State the blood parasite species.
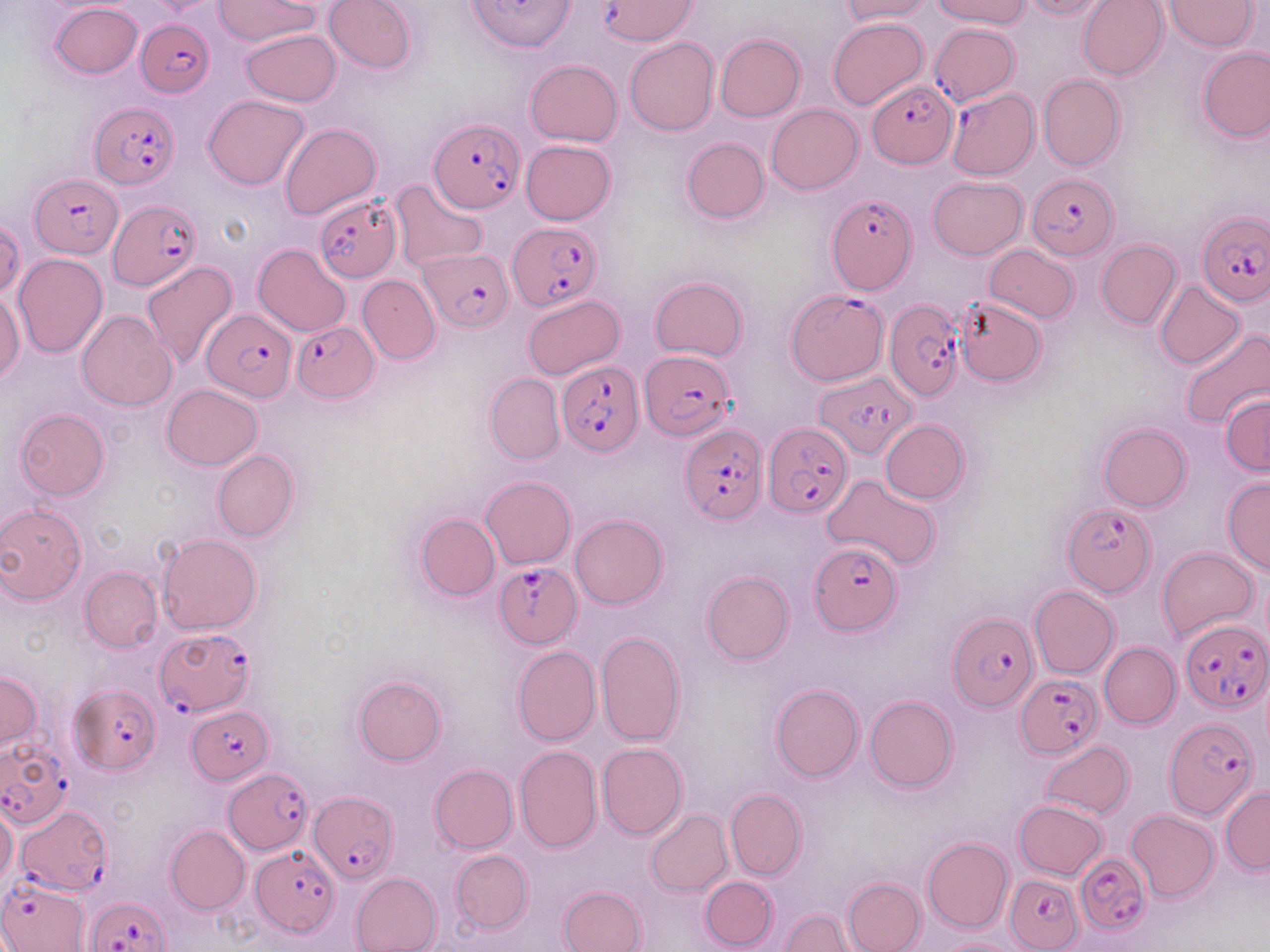

Plasmodium falciparum.

stain = May-Grünwald-Giemsa
image size = 1270×952 pixels
field of view = single
modality = light microscopy
Plasmodium falciparum-infected red blood cell locations = approximate bounding boxes as (x1,y1)-(x2,y2) corner pairs in pixels: (597,2)-(698,50), (136,18)-(213,98), (929,23)-(1019,105), (867,79)-(956,166), (946,88)-(1038,180), (88,101)-(180,188), (429,118)-(525,214), (1027,173)-(1119,260), (32,174)-(123,257), (313,194)-(402,281), (828,194)-(917,295), (109,199)-(200,290), (1198,214)-(1269,306), (507,223)-(600,311), (421,247)-(511,331), (785,290)-(889,385), (884,298)-(967,401), (201,308)-(298,401), (294,322)-(376,402), (643,351)-(735,441), (555,359)-(644,456), (815,375)-(915,459), (763,421)-(852,519), (680,424)-(767,523), (1062,502)-(1156,596), (809,544)-(902,634), (494,563)-(582,648), (950,612)-(1037,711), (1179,616)-(1269,715), (156,628)-(255,716), (1015,674)-(1103,757), (70,684)-(160,773), (188,705)-(271,786), (1162,717)-(1260,820), (0,739)-(69,831), (224,768)-(312,853), (307,792)-(397,884), (13,804)-(111,895), (251,846)-(337,937), (1076,852)-(1150,935), (1006,873)-(1084,949), (1,879)-(89,951), (87,896)-(171,951)
preparation = thin blood smear
uninfected red blood cell locations = approximate bounding boxes as (x1,y1)-(x2,y2) corner pairs in pixels: (212,0)-(320,46), (324,0)-(416,73), (838,0)-(933,23), (931,0)-(1029,27), (1017,0)-(1111,20), (1078,0)-(1168,80), (1164,1)-(1261,51), (49,3)-(142,79), (829,18)-(928,110), (241,29)-(340,107), (714,33)-(805,121), (624,38)-(718,136), (1197,46)-(1269,142), (525,60)-(622,146), (1038,75)-(1126,171), (203,95)-(309,189), (766,104)-(862,195), (279,123)-(380,220), (682,137)-(769,223), (521,140)-(615,225), (928,177)-(1028,258), (389,180)-(488,273), (1,218)-(23,300), (1096,239)-(1181,328), (253,244)-(350,336), (984,245)-(1079,322), (14,254)-(108,358), (141,259)-(238,370), (358,275)-(440,364), (651,275)-(748,361), (1155,280)-(1245,369), (0,291)-(24,383), (523,295)-(624,379), (954,297)-(1046,386), (76,309)-(176,411), (1178,329)-(1270,429), (485,373)-(564,464), (162,383)-(261,470), (1220,394)-(1270,477), (15,409)-(108,500), (881,419)-(969,503), (1098,423)-(1191,512), (212,450)-(298,541), (481,475)-(575,569), (822,476)-(942,571), (1222,478)-(1270,575), (0,504)-(87,604), (414,513)-(500,602), (570,514)-(669,609), (158,533)-(261,634), (1158,546)-(1258,641), (80,567)-(163,651), (702,571)-(794,665), (1029,585)-(1119,678), (596,631)-(686,746), (1099,643)-(1180,729), (512,646)-(601,746), (0,669)-(40,752), (353,676)-(446,766), (771,684)-(864,783), (864,694)-(958,792), (1040,741)-(1133,819), (597,742)-(687,839), (515,745)-(603,852), (430,763)-(517,853), (1220,785)-(1269,874), (725,788)-(806,881), (1014,800)-(1107,880), (0,806)-(17,886), (644,809)-(732,897), (1125,809)-(1219,901), (165,825)-(250,915), (922,837)-(1013,933), (451,850)-(531,934), (350,872)-(441,952), (701,877)-(778,949), (842,877)-(925,952), (559,884)-(647,952), (778,909)-(864,951), (937,936)-(1024,952)
magnification = 1000x